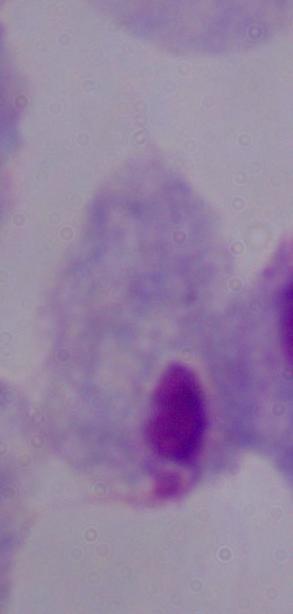
Summary:
  - Modality: photomicrograph
  - Identification: trichomonad
  - Magnification: 1000x